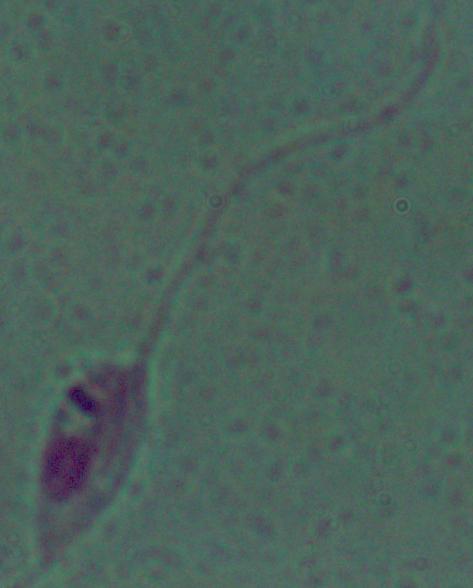 Micrograph. A Leishmania parasite is shown. 1000x magnification.